Point out every Plasmodium parasite.
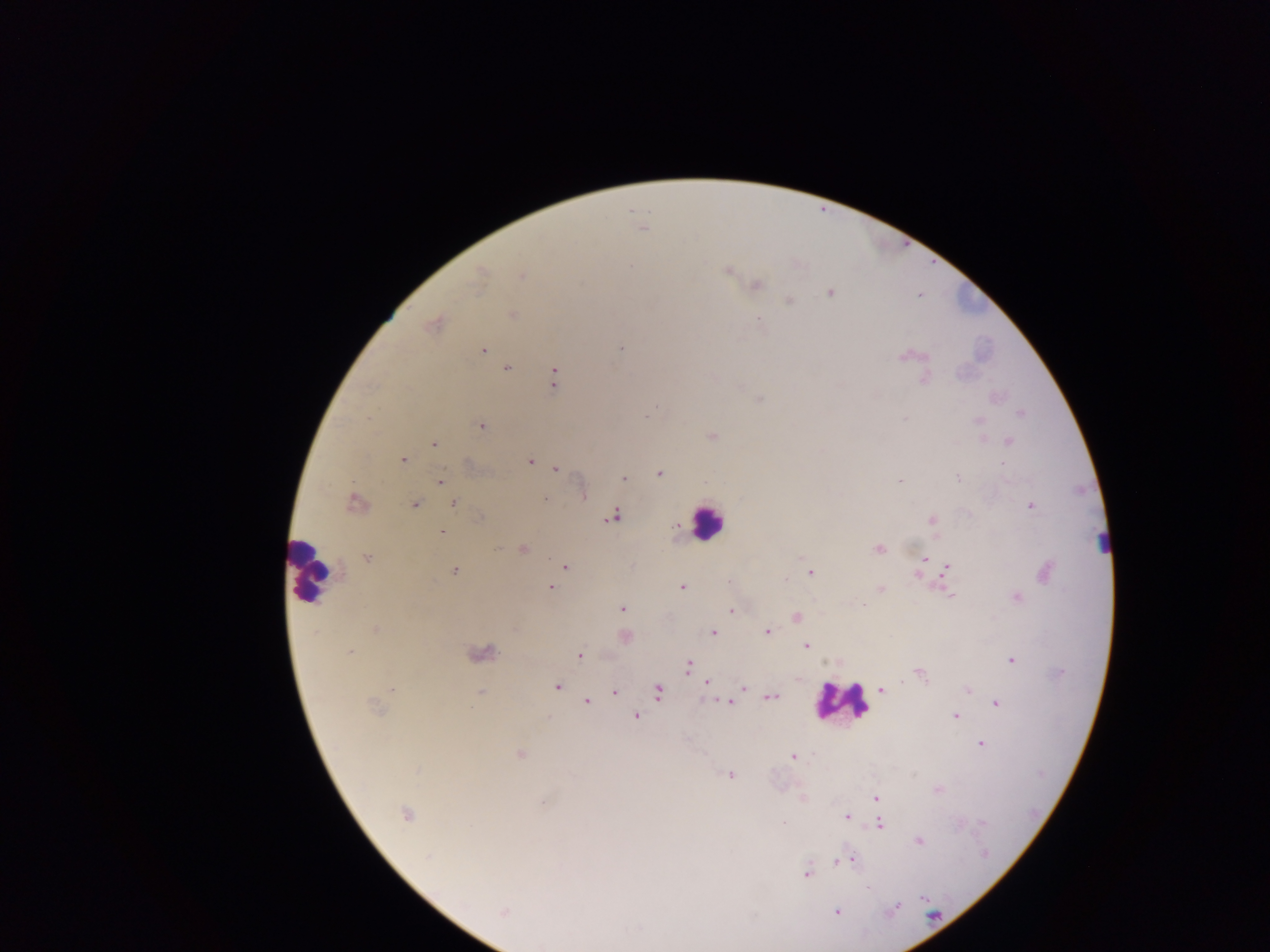
Approximate centers as [x, y] in pixels.
Plasmodium parasites: [642, 228], [631, 267], [727, 270], [521, 275], [478, 280], [756, 286], [830, 293], [789, 300], [513, 315], [759, 319], [433, 324], [620, 348], [482, 349], [903, 356], [507, 368], [554, 378], [924, 380], [1020, 414], [978, 421], [481, 426], [713, 437], [1009, 441], [434, 444], [403, 460], [530, 461], [1002, 463], [556, 469], [659, 474], [623, 478], [958, 478], [440, 479], [900, 481], [584, 496], [546, 499], [354, 503], [415, 504], [453, 504], [1030, 506], [613, 516], [932, 520], [442, 532], [499, 548], [878, 548], [523, 549], [367, 557], [925, 559], [565, 566], [947, 567], [455, 571], [810, 573], [785, 579], [551, 587], [682, 587], [881, 589], [948, 594], [1017, 598], [622, 609], [732, 610], [797, 617], [377, 629], [713, 632], [767, 632], [625, 637], [806, 645], [350, 651], [484, 653], [579, 656], [1011, 659], [687, 666], [919, 674], [707, 683], [557, 687], [743, 687], [968, 689], [392, 690], [881, 690], [614, 691], [480, 692], [658, 692], [772, 697], [587, 702], [730, 703], [997, 704], [375, 707], [636, 716], [956, 716], [981, 744], [520, 754], [792, 756], [417, 769], [731, 775], [877, 798], [542, 802], [405, 814], [846, 817], [784, 823], [880, 824], [919, 841], [428, 857], [850, 859], [840, 860], [806, 874], [867, 888], [896, 908], [503, 912], [837, 912], [542, 946].

image size = 1270×952 pixels
preparation = thick blood film
country = Ghana
leukocyte locations = approximate centers as [x, y] in pixels: [707, 522], [310, 569], [840, 701]
capture = mobile-phone photograph through a microscope
field of view = single